Locate and identify every blood parasite.
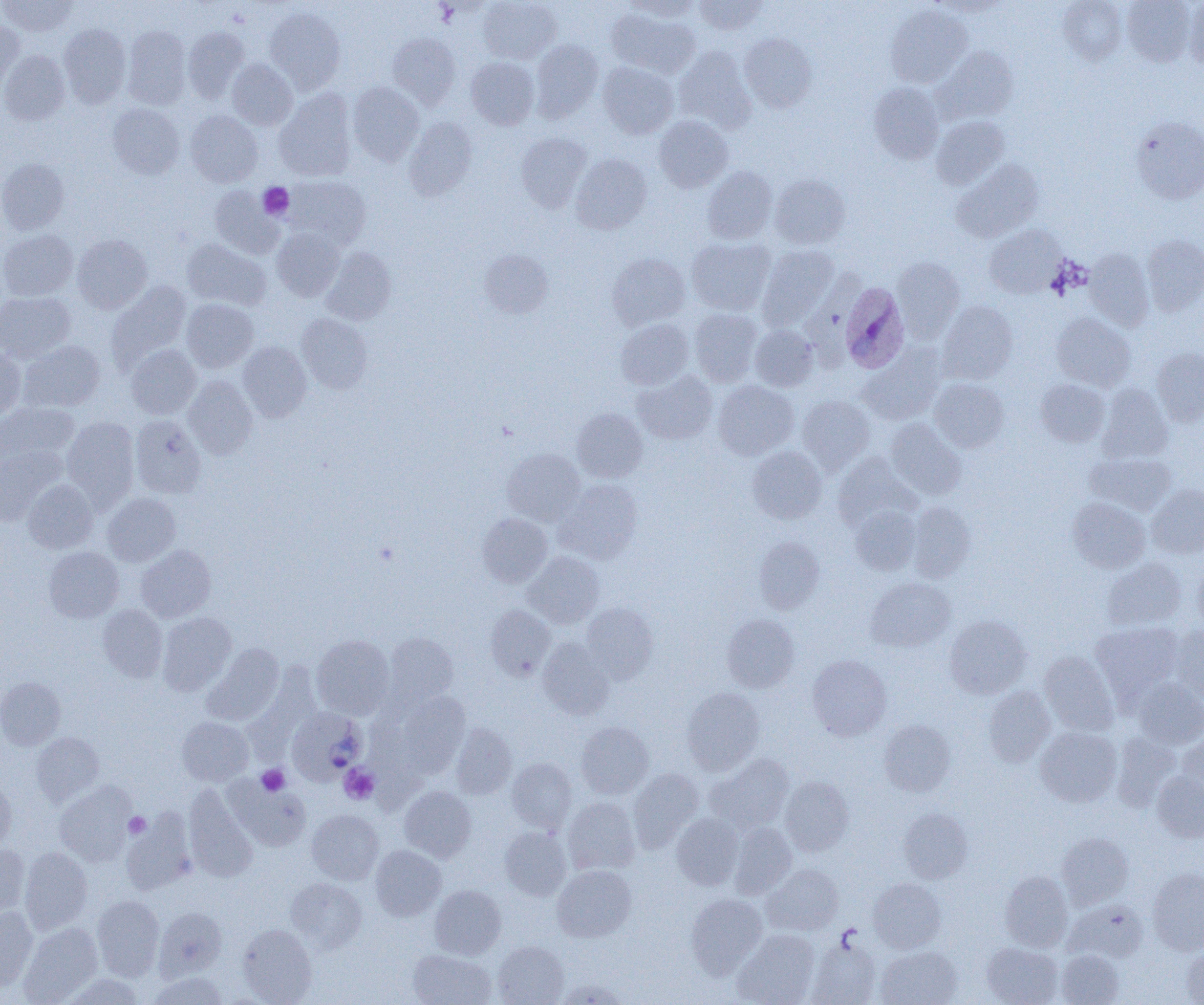

Approximate bounding boxes as named x1/y1/x2/y2 corners in pixels.
Plasmodium ovale-infected red blood cells: (x1=839, y1=283, x2=909, y2=373), (x1=287, y1=706, x2=368, y2=785).
No Plasmodium falciparum, Plasmodium malariae, Plasmodium vivax, Babesia divergens, or Trypanosoma brucei observed.

Uninfected red blood cell locations: (x1=1, y1=0, x2=78, y2=37), (x1=478, y1=0, x2=561, y2=64), (x1=624, y1=0, x2=701, y2=21), (x1=693, y1=0, x2=767, y2=35), (x1=929, y1=0, x2=1011, y2=17), (x1=1122, y1=0, x2=1195, y2=66), (x1=1057, y1=1, x2=1127, y2=65), (x1=1183, y1=1, x2=1204, y2=70), (x1=885, y1=4, x2=972, y2=89), (x1=264, y1=7, x2=345, y2=93), (x1=606, y1=8, x2=700, y2=77), (x1=0, y1=20, x2=24, y2=93), (x1=58, y1=23, x2=131, y2=107), (x1=122, y1=25, x2=191, y2=109), (x1=183, y1=27, x2=249, y2=103), (x1=387, y1=33, x2=460, y2=109), (x1=740, y1=33, x2=816, y2=113), (x1=530, y1=39, x2=603, y2=121), (x1=674, y1=46, x2=755, y2=133), (x1=934, y1=46, x2=1018, y2=124), (x1=0, y1=51, x2=69, y2=125), (x1=466, y1=57, x2=539, y2=129), (x1=227, y1=59, x2=297, y2=130), (x1=598, y1=61, x2=678, y2=139), (x1=347, y1=82, x2=424, y2=166), (x1=868, y1=83, x2=944, y2=164), (x1=274, y1=89, x2=357, y2=181), (x1=107, y1=103, x2=184, y2=179), (x1=185, y1=110, x2=262, y2=187), (x1=653, y1=116, x2=732, y2=192), (x1=931, y1=116, x2=1009, y2=189), (x1=405, y1=117, x2=477, y2=202), (x1=1131, y1=117, x2=1204, y2=204), (x1=516, y1=132, x2=591, y2=212), (x1=571, y1=154, x2=652, y2=234), (x1=0, y1=158, x2=69, y2=234), (x1=952, y1=159, x2=1044, y2=242), (x1=702, y1=166, x2=778, y2=244), (x1=769, y1=174, x2=850, y2=249), (x1=284, y1=176, x2=371, y2=249), (x1=209, y1=186, x2=284, y2=259), (x1=984, y1=225, x2=1065, y2=299), (x1=272, y1=228, x2=345, y2=301), (x1=0, y1=230, x2=77, y2=301), (x1=72, y1=234, x2=153, y2=313), (x1=1141, y1=234, x2=1204, y2=316), (x1=687, y1=237, x2=776, y2=315), (x1=182, y1=239, x2=271, y2=310), (x1=756, y1=245, x2=838, y2=330), (x1=321, y1=248, x2=396, y2=326), (x1=1085, y1=248, x2=1154, y2=330), (x1=478, y1=249, x2=553, y2=317), (x1=607, y1=254, x2=690, y2=329), (x1=891, y1=257, x2=964, y2=340), (x1=107, y1=282, x2=191, y2=370), (x1=0, y1=292, x2=74, y2=362), (x1=181, y1=299, x2=258, y2=372), (x1=937, y1=301, x2=1018, y2=384), (x1=689, y1=308, x2=762, y2=386), (x1=296, y1=313, x2=372, y2=393), (x1=1052, y1=313, x2=1135, y2=390), (x1=615, y1=319, x2=693, y2=389), (x1=749, y1=324, x2=818, y2=391), (x1=19, y1=340, x2=105, y2=412), (x1=238, y1=341, x2=312, y2=421), (x1=126, y1=344, x2=200, y2=418), (x1=0, y1=347, x2=26, y2=418), (x1=858, y1=347, x2=945, y2=425), (x1=1151, y1=348, x2=1204, y2=426), (x1=633, y1=371, x2=717, y2=444), (x1=184, y1=376, x2=257, y2=459), (x1=928, y1=378, x2=1008, y2=452), (x1=1035, y1=379, x2=1109, y2=446), (x1=713, y1=380, x2=798, y2=460), (x1=1098, y1=383, x2=1173, y2=462), (x1=797, y1=395, x2=875, y2=474), (x1=0, y1=402, x2=79, y2=462), (x1=571, y1=408, x2=648, y2=482), (x1=130, y1=415, x2=206, y2=499), (x1=61, y1=417, x2=139, y2=507), (x1=885, y1=419, x2=966, y2=500), (x1=0, y1=446, x2=64, y2=525), (x1=747, y1=446, x2=827, y2=523), (x1=503, y1=449, x2=584, y2=525), (x1=832, y1=452, x2=919, y2=529), (x1=1085, y1=452, x2=1175, y2=515), (x1=555, y1=479, x2=642, y2=563), (x1=23, y1=480, x2=98, y2=552), (x1=1147, y1=485, x2=1204, y2=558), (x1=103, y1=493, x2=180, y2=566), (x1=1068, y1=498, x2=1150, y2=573), (x1=907, y1=501, x2=975, y2=581), (x1=850, y1=506, x2=920, y2=575), (x1=477, y1=513, x2=552, y2=587), (x1=754, y1=536, x2=824, y2=614), (x1=136, y1=545, x2=215, y2=622), (x1=44, y1=547, x2=123, y2=622), (x1=523, y1=552, x2=603, y2=628), (x1=1102, y1=558, x2=1187, y2=631), (x1=1193, y1=563, x2=1204, y2=632), (x1=866, y1=577, x2=955, y2=652), (x1=581, y1=602, x2=657, y2=683), (x1=98, y1=604, x2=167, y2=682), (x1=485, y1=605, x2=556, y2=680), (x1=157, y1=613, x2=236, y2=695), (x1=722, y1=613, x2=800, y2=693), (x1=944, y1=615, x2=1031, y2=698), (x1=1091, y1=622, x2=1183, y2=703), (x1=1170, y1=626, x2=1204, y2=705), (x1=384, y1=633, x2=459, y2=708), (x1=312, y1=635, x2=394, y2=719), (x1=537, y1=637, x2=614, y2=720), (x1=203, y1=643, x2=284, y2=726), (x1=1040, y1=651, x2=1118, y2=735), (x1=807, y1=655, x2=891, y2=740), (x1=0, y1=677, x2=65, y2=750), (x1=1133, y1=678, x2=1204, y2=749), (x1=983, y1=686, x2=1055, y2=767), (x1=682, y1=687, x2=765, y2=774), (x1=396, y1=692, x2=470, y2=777), (x1=177, y1=717, x2=253, y2=785), (x1=879, y1=720, x2=956, y2=796), (x1=576, y1=722, x2=654, y2=799), (x1=451, y1=723, x2=516, y2=799), (x1=1035, y1=727, x2=1121, y2=807), (x1=32, y1=732, x2=104, y2=806), (x1=1177, y1=732, x2=1204, y2=803), (x1=1112, y1=733, x2=1181, y2=811), (x1=707, y1=755, x2=794, y2=832), (x1=506, y1=758, x2=576, y2=832), (x1=627, y1=769, x2=703, y2=852), (x1=1152, y1=770, x2=1204, y2=842), (x1=0, y1=776, x2=16, y2=850), (x1=225, y1=776, x2=311, y2=852), (x1=780, y1=776, x2=853, y2=856), (x1=54, y1=782, x2=136, y2=866), (x1=183, y1=785, x2=258, y2=883), (x1=399, y1=786, x2=476, y2=862), (x1=563, y1=797, x2=640, y2=874), (x1=898, y1=807, x2=972, y2=883), (x1=307, y1=810, x2=384, y2=884), (x1=121, y1=811, x2=196, y2=895), (x1=672, y1=813, x2=744, y2=889), (x1=729, y1=822, x2=796, y2=898), (x1=499, y1=827, x2=571, y2=900), (x1=1057, y1=832, x2=1133, y2=908), (x1=0, y1=844, x2=30, y2=919), (x1=370, y1=845, x2=446, y2=921), (x1=19, y1=847, x2=93, y2=934), (x1=762, y1=864, x2=843, y2=935), (x1=552, y1=865, x2=636, y2=941), (x1=1147, y1=868, x2=1204, y2=954), (x1=999, y1=871, x2=1073, y2=951), (x1=285, y1=878, x2=367, y2=952), (x1=868, y1=879, x2=946, y2=952), (x1=430, y1=885, x2=506, y2=959), (x1=685, y1=893, x2=767, y2=977), (x1=92, y1=895, x2=164, y2=980), (x1=1064, y1=901, x2=1147, y2=963), (x1=0, y1=906, x2=38, y2=991), (x1=154, y1=907, x2=227, y2=979), (x1=19, y1=922, x2=102, y2=1004), (x1=237, y1=924, x2=317, y2=1004), (x1=733, y1=930, x2=819, y2=1005), (x1=806, y1=936, x2=881, y2=1005), (x1=493, y1=940, x2=568, y2=1005), (x1=982, y1=942, x2=1062, y2=1005), (x1=1182, y1=946, x2=1204, y2=1005), (x1=876, y1=947, x2=961, y2=1005), (x1=408, y1=949, x2=496, y2=1005), (x1=1056, y1=950, x2=1123, y2=1005), (x1=147, y1=972, x2=231, y2=1005), (x1=61, y1=973, x2=146, y2=1004), (x1=555, y1=979, x2=629, y2=1004). Platelet locations: (x1=258, y1=182, x2=294, y2=220), (x1=340, y1=764, x2=379, y2=804), (x1=256, y1=765, x2=290, y2=796), (x1=124, y1=812, x2=151, y2=838). Slide-level diagnosis: Plasmodium ovale. Single field of view. Captured at 1000x magnification. Image is 1204×1005 pixels. Thin blood smear. Light microscopy.